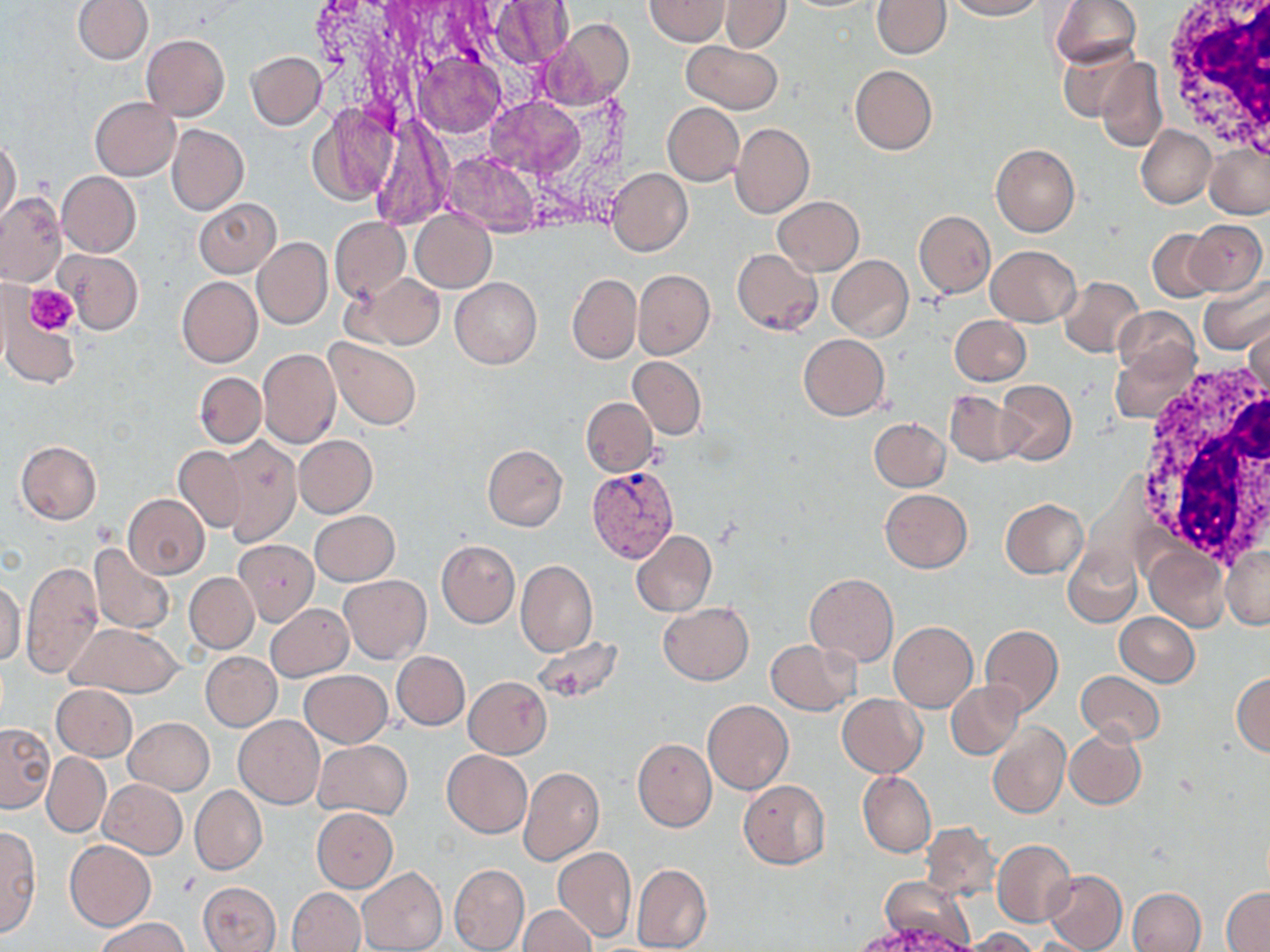
Approximate bounding boxes as (x1,y1)-(x2,y2) corner pairs in pixels. Plasmodium vivax-infected red blood cell locations: (588,466)-(680,565). Platelet locations: (25,284)-(78,335). White blood cell locations: (1156,0)-(1270,155), (1133,360)-(1270,570). Uninfected red blood cell locations: (73,0)-(152,64), (645,0)-(730,46), (945,0)-(1042,20), (1050,0)-(1142,70), (487,1)-(576,69), (718,1)-(791,53), (871,1)-(950,58), (545,20)-(634,108), (141,34)-(230,120), (681,39)-(782,115), (1057,44)-(1141,123), (246,51)-(326,129), (1095,56)-(1166,153), (850,64)-(937,154), (90,97)-(180,180), (313,103)-(401,206), (662,103)-(744,185), (100,112)-(246,200), (366,116)-(451,231), (730,122)-(814,219), (166,123)-(248,215), (1136,124)-(1216,209), (0,137)-(21,224), (1204,141)-(1269,218), (991,143)-(1079,236), (607,168)-(692,255), (56,171)-(141,257), (0,192)-(66,286), (773,196)-(864,275), (194,198)-(281,277), (410,210)-(496,293), (915,212)-(995,297), (329,216)-(410,302), (1189,219)-(1267,294), (1148,229)-(1219,303), (252,237)-(332,329), (986,245)-(1079,325), (59,249)-(143,334), (732,249)-(822,335), (827,255)-(912,342), (633,270)-(714,359), (351,272)-(445,350), (568,274)-(639,362), (176,276)-(262,367), (1058,276)-(1145,358), (451,277)-(542,368), (1199,280)-(1270,355), (1113,307)-(1200,385), (2,309)-(80,388), (949,314)-(1031,385), (1244,318)-(1269,401), (798,333)-(890,420), (326,337)-(422,431), (1110,343)-(1196,424), (257,349)-(340,448), (629,356)-(705,439), (195,372)-(266,447), (995,381)-(1076,466), (945,389)-(1022,466), (581,397)-(657,476), (869,418)-(950,492), (294,435)-(377,517), (216,437)-(302,546), (16,440)-(102,524), (483,444)-(568,532), (172,445)-(249,534), (880,489)-(972,573), (122,495)-(209,578), (1000,499)-(1087,577), (310,511)-(399,586), (630,529)-(717,617), (233,540)-(320,626), (437,540)-(519,627), (90,542)-(175,634), (1144,543)-(1229,631), (1063,545)-(1142,629), (1221,546)-(1270,629), (20,559)-(103,678), (516,559)-(597,657), (184,572)-(259,653), (805,572)-(898,666), (339,575)-(431,663), (0,581)-(26,665), (659,601)-(753,684), (265,604)-(354,681), (1115,612)-(1199,686), (888,621)-(977,711), (64,623)-(185,698), (979,625)-(1063,716), (532,635)-(623,703), (766,639)-(859,715), (201,651)-(282,731), (392,651)-(469,730), (299,670)-(392,748), (1076,671)-(1165,747), (1231,672)-(1270,758), (464,676)-(553,758), (946,681)-(1025,759), (51,684)-(139,761), (837,693)-(926,777), (703,699)-(793,794), (234,715)-(325,809), (123,717)-(214,795), (1,722)-(55,811), (987,722)-(1068,819), (1064,728)-(1147,809), (632,737)-(717,833), (313,740)-(413,819), (441,750)-(533,837), (43,753)-(111,837), (42,766)-(183,846), (518,766)-(604,865), (858,771)-(936,857), (100,779)-(187,859), (738,780)-(831,869), (190,785)-(266,876), (311,808)-(397,891), (920,822)-(1000,902), (0,826)-(41,937), (64,839)-(156,931), (993,839)-(1077,928), (553,846)-(636,942), (449,863)-(529,952), (631,863)-(712,952), (358,866)-(447,952), (1043,869)-(1128,952), (877,878)-(973,951), (198,881)-(280,952), (287,887)-(366,952), (1222,887)-(1270,950), (1127,888)-(1206,952), (517,905)-(596,952), (94,915)-(190,952), (964,928)-(1041,951). Slide-level diagnosis: Plasmodium vivax. Image is 1270×952 pixels. One field of a larger specimen. May-Grünwald-Giemsa-stained preparation. Thin blood film. 1000x magnification. Light microscopy.